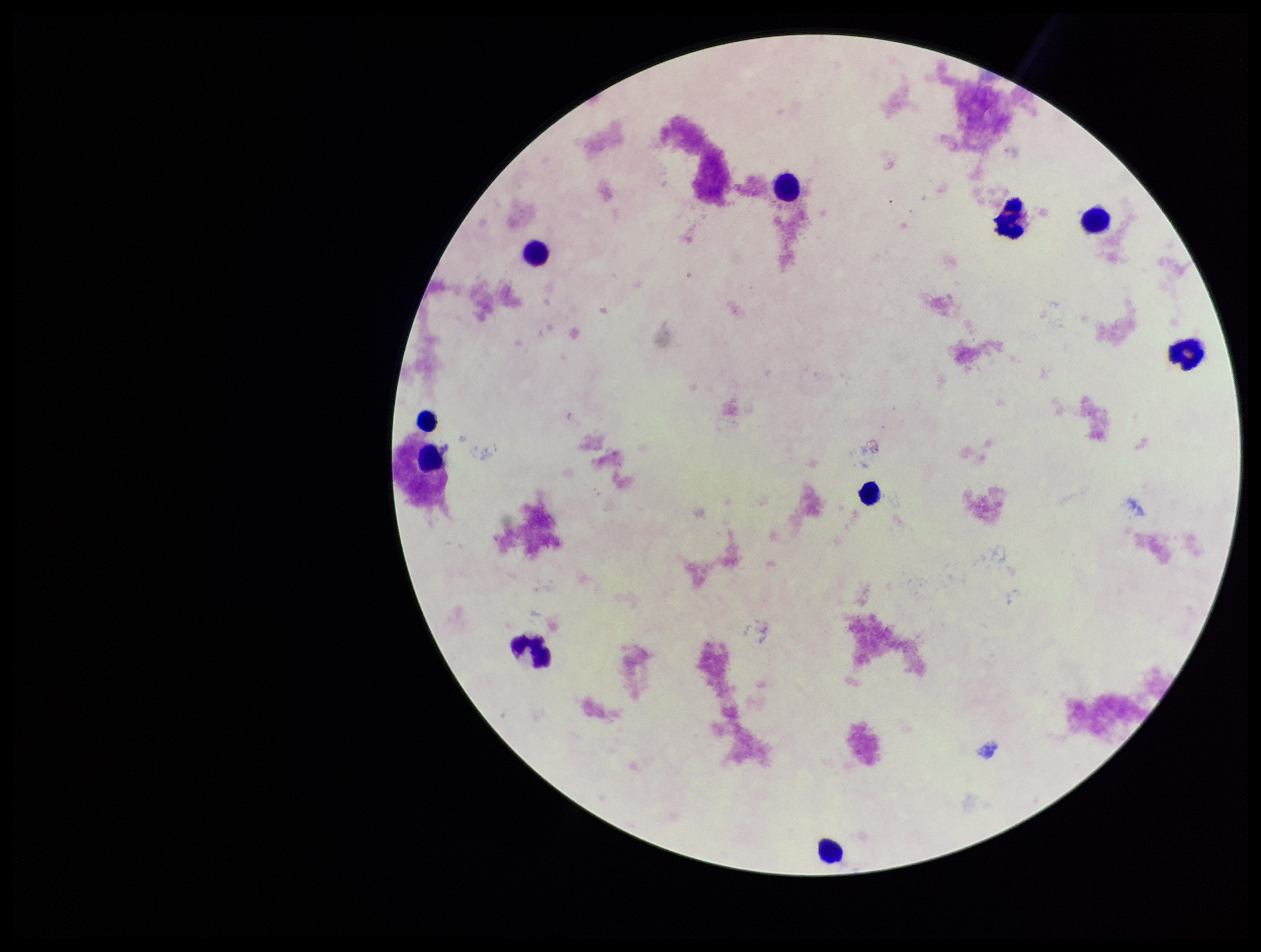

One field from this slide. Plasmodium parasites: none identified. Leukocyte count: 10. Smartphone photograph taken through the eyepiece of a microscope. Preparation: thick smear. Image is 1261×952 pixels. Giemsa stain. Parasite count: 0. Patient malaria status: negative.